Locate every malaria parasite and every leukocyte.
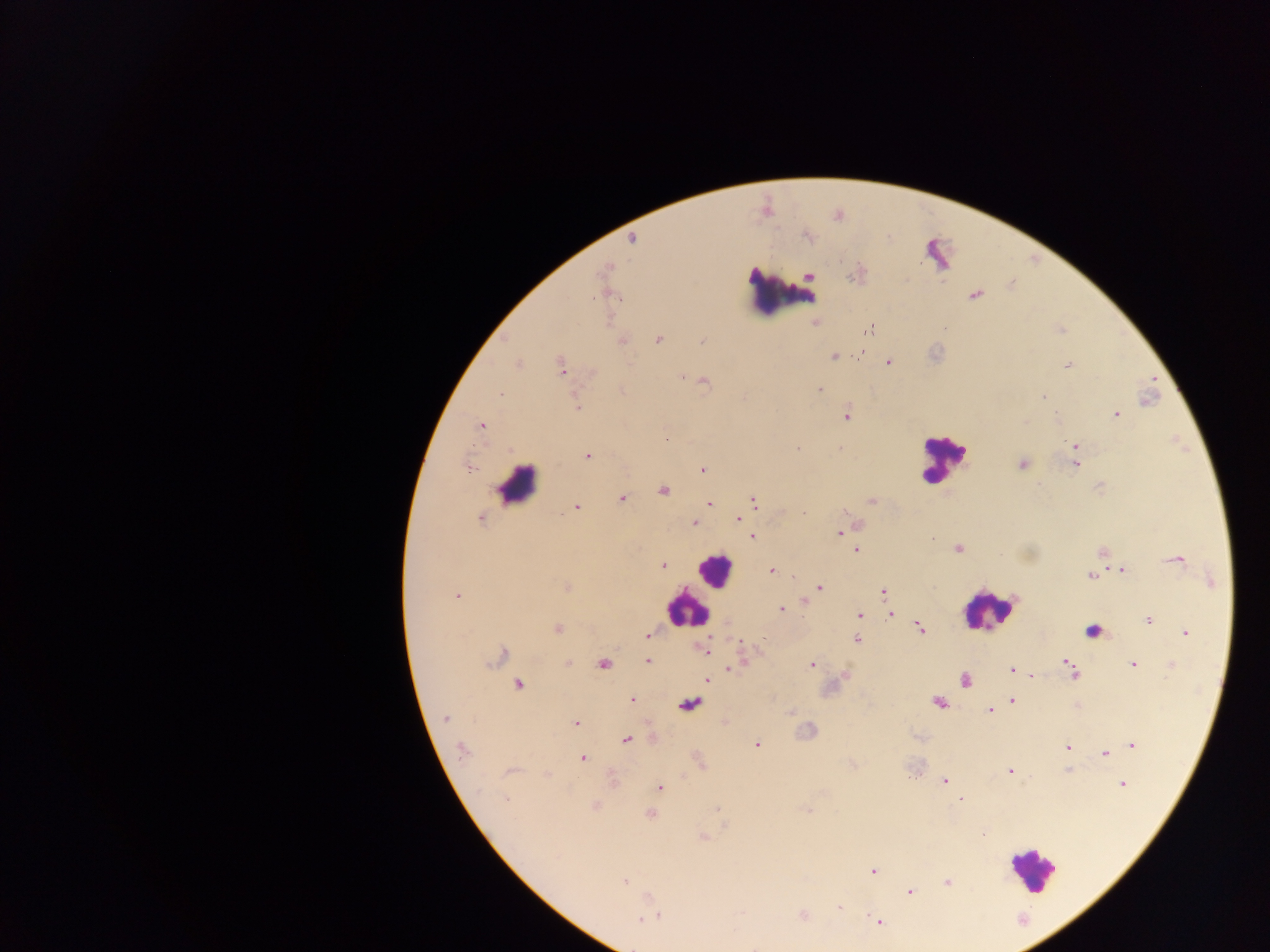

Approximate centers as {x, y} in pixels.
Malaria parasites: {633, 239}, {810, 277}, {853, 277}, {975, 295}, {592, 297}, {945, 328}, {869, 330}, {658, 340}, {622, 341}, {701, 342}, {859, 353}, {833, 356}, {888, 362}, {518, 365}, {1068, 365}, {561, 367}, {682, 378}, {704, 382}, {819, 389}, {501, 394}, {1043, 396}, {577, 407}, {1116, 414}, {847, 415}, {482, 427}, {666, 438}, {1075, 446}, {798, 449}, {587, 456}, {1021, 464}, {1076, 465}, {469, 468}, {702, 469}, {663, 491}, {621, 498}, {872, 501}, {754, 502}, {709, 504}, {576, 507}, {804, 513}, {480, 519}, {739, 520}, {694, 523}, {839, 533}, {752, 537}, {932, 538}, {958, 548}, {856, 550}, {1101, 552}, {1177, 560}, {664, 565}, {771, 570}, {1123, 570}, {1091, 575}, {1212, 581}, {566, 587}, {820, 588}, {883, 593}, {457, 595}, {806, 603}, {781, 609}, {891, 614}, {859, 615}, {1148, 620}, {920, 627}, {557, 628}, {1185, 633}, {647, 634}, {856, 639}, {738, 641}, {704, 650}, {502, 656}, {647, 660}, {1066, 662}, {569, 663}, {742, 663}, {603, 664}, {1134, 664}, {811, 665}, {1171, 666}, {1071, 667}, {734, 668}, {1011, 670}, {1073, 673}, {845, 675}, {1031, 675}, {708, 680}, {965, 680}, {518, 684}, {632, 699}, {1012, 701}, {937, 703}, {689, 704}, {990, 710}, {791, 713}, {445, 718}, {576, 722}, {626, 740}, {757, 745}, {1132, 745}, {1067, 746}, {461, 751}, {1104, 754}, {583, 759}, {1009, 770}, {509, 772}, {944, 781}, {1122, 784}, {660, 787}, {960, 798}, {506, 799}, {595, 806}, {717, 809}, {808, 811}, {650, 813}, {703, 838}, {873, 871}, {625, 882}, {947, 882}, {909, 892}, {839, 907}, {803, 915}, {652, 916}, {642, 919}, {878, 921}.
Leukocytes: {782, 291}, {942, 458}, {518, 484}, {714, 569}, {687, 610}, {988, 611}, {1089, 631}, {1032, 869}.

Summary:
  - Capture: mobile-phone photograph through a microscope
  - Country: Ghana
  - Preparation: thick blood smear
  - Field of view: single
  - Image size: 1270×952 pixels